State which parasite is depicted.
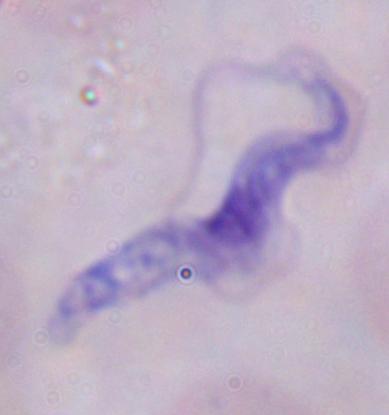
This is a trypanosome.

magnification = 1000x
modality = micrograph